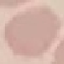

Summary:
  - Result: negative for malaria parasites
  - Capture: smartphone camera at the microscope eyepiece
  - Preparation: thin smear
  - Image type: cell patch, automatically extracted from a larger field of view and resized to 64 × 64 pixels
  - Stain: Giemsa